Look for Plasmodium parasites.
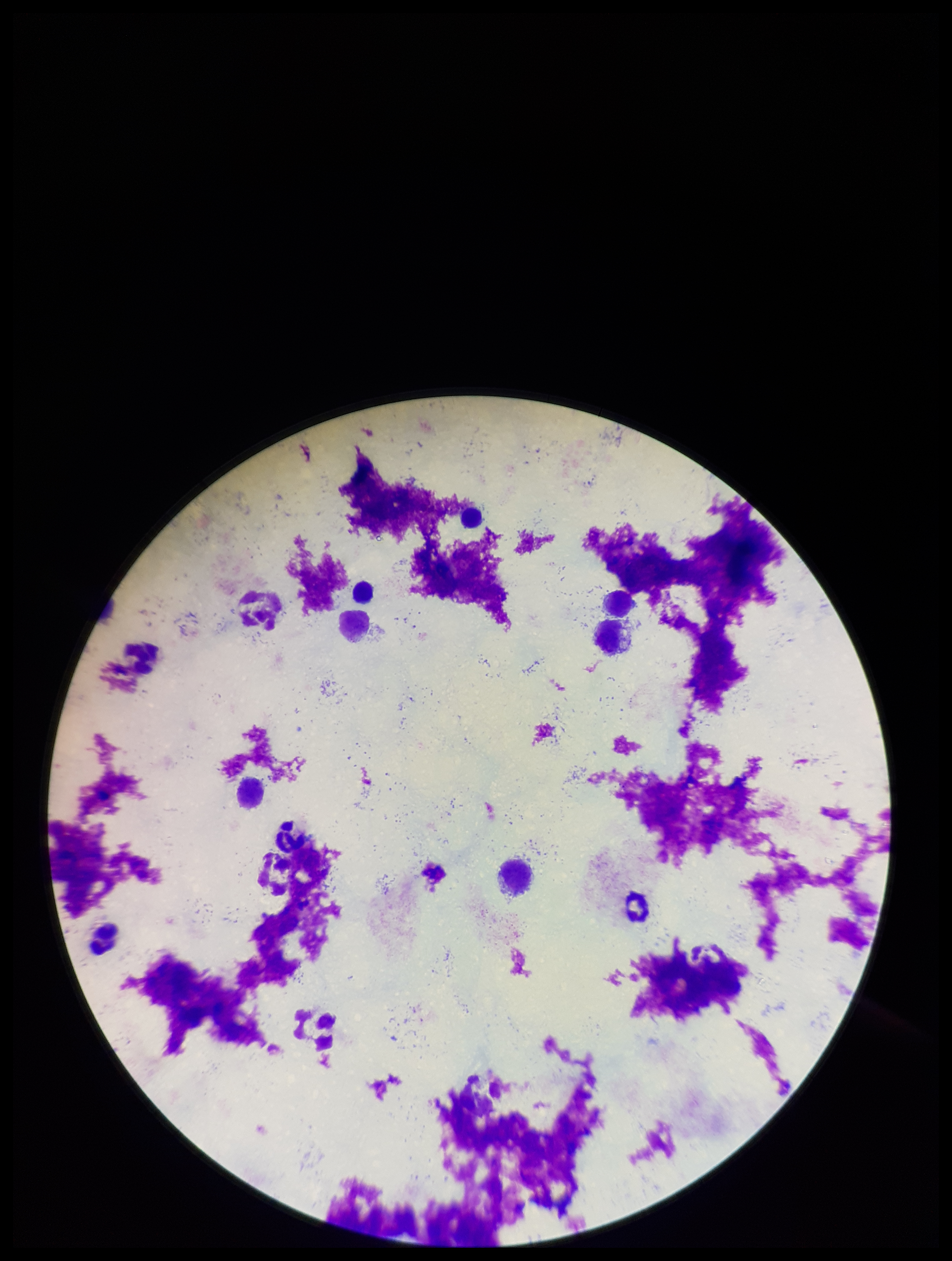

None seen.

preparation = thick
capture = smartphone photograph through the microscope eyepiece
field of view = single
parasite count = 0
stain = Giemsa
image size = 952×1261 pixels
leukocyte count = 9
patient malaria status = negative